Outline each Trypanosoma brucei.
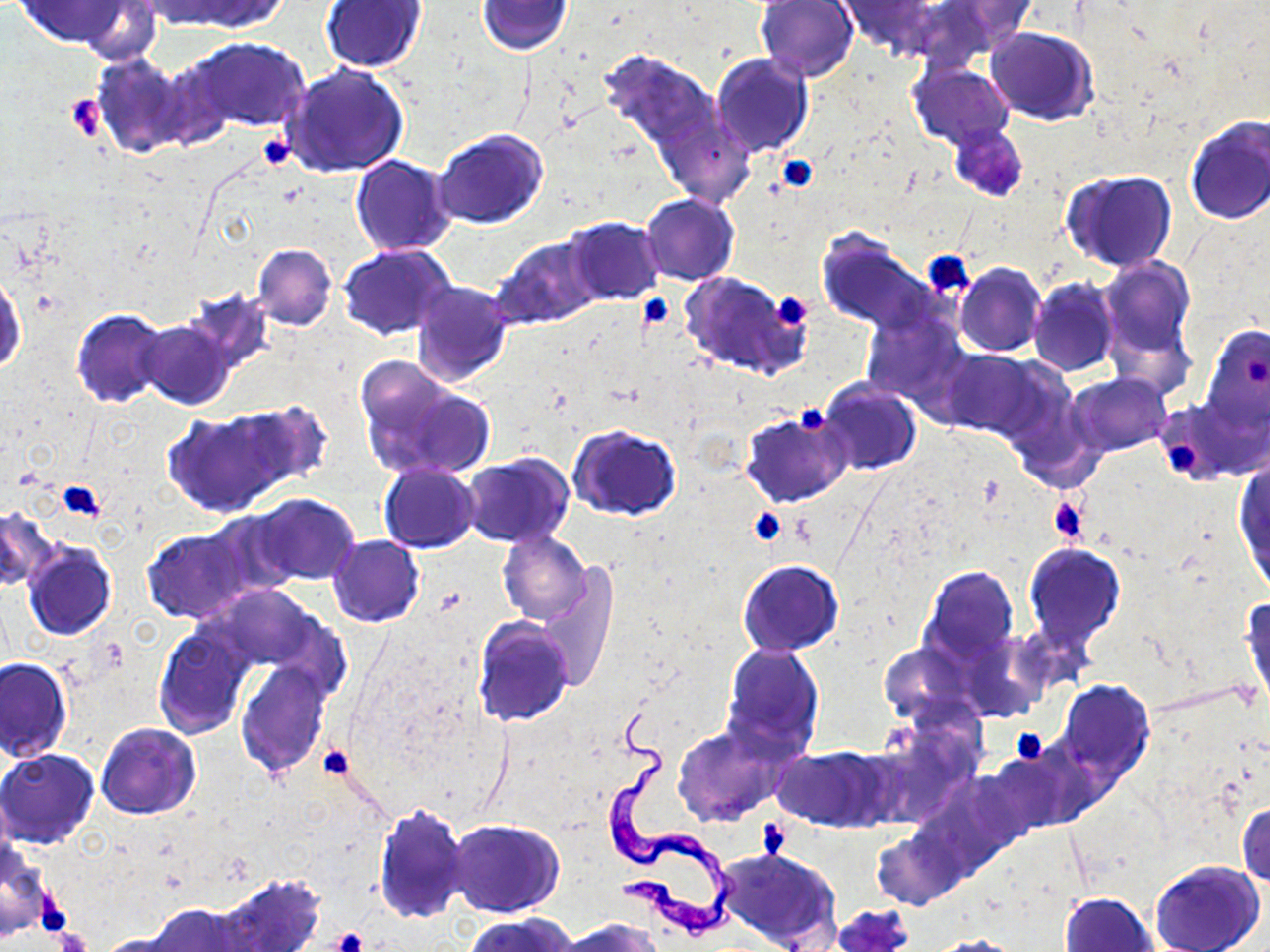

Approximate bounding boxes as (x1, y1, x2, y2) in pixels.
Trypanosoma brucei: (598, 703, 735, 935).

Summary:
  - Uninfected red blood cell locations: (14, 0, 135, 48), (137, 0, 252, 28), (173, 0, 292, 33), (478, 0, 575, 55), (755, 0, 859, 82), (944, 0, 1037, 48), (318, 1, 428, 73), (836, 1, 938, 55), (900, 1, 1021, 62), (74, 2, 163, 66), (985, 26, 1098, 124), (182, 36, 309, 132), (597, 49, 724, 155), (710, 52, 813, 159), (90, 53, 193, 157), (281, 63, 409, 178), (908, 63, 1014, 152), (655, 103, 754, 211), (1184, 115, 1270, 226), (950, 124, 1028, 202), (433, 131, 547, 230), (350, 154, 457, 256), (1062, 169, 1178, 271), (641, 193, 739, 286), (564, 216, 663, 304), (817, 230, 939, 336), (493, 235, 603, 327), (252, 244, 337, 330), (339, 244, 456, 339), (1099, 256, 1196, 369), (955, 263, 1046, 357), (0, 272, 26, 374), (679, 272, 808, 378), (1028, 277, 1119, 377), (410, 280, 514, 387), (181, 289, 276, 380), (72, 307, 171, 409), (861, 308, 970, 406), (138, 321, 234, 409), (1199, 324, 1270, 438), (939, 349, 1042, 439), (354, 363, 493, 482), (1065, 373, 1173, 457), (815, 378, 921, 477), (164, 407, 299, 517), (741, 409, 850, 508), (568, 424, 681, 520), (1234, 450, 1270, 594), (461, 454, 574, 547), (378, 462, 480, 553), (249, 494, 360, 585), (0, 505, 57, 593), (205, 508, 308, 598), (143, 528, 252, 623), (498, 530, 591, 624), (328, 535, 424, 627), (22, 540, 116, 640), (1023, 544, 1126, 651), (737, 559, 843, 656), (536, 564, 618, 692), (919, 564, 1021, 666), (205, 583, 330, 674), (1241, 593, 1269, 712), (472, 616, 575, 725), (153, 623, 255, 740), (879, 640, 977, 726), (721, 644, 824, 757), (0, 658, 73, 762), (234, 661, 331, 778), (1055, 678, 1154, 782), (96, 722, 201, 819), (672, 723, 789, 827), (776, 746, 890, 832), (0, 749, 102, 849), (988, 754, 1084, 836), (1236, 797, 1270, 887), (372, 803, 472, 925), (448, 819, 564, 918), (869, 825, 965, 911), (0, 845, 49, 941), (716, 847, 840, 952), (1149, 859, 1266, 952), (213, 873, 325, 952), (1060, 890, 1161, 951), (143, 901, 255, 952), (465, 913, 577, 952), (560, 917, 660, 952), (93, 930, 196, 952), (925, 935, 1028, 952)
  - Platelet locations: (65, 94, 103, 140), (256, 134, 297, 172), (775, 154, 818, 193), (922, 250, 974, 296), (771, 292, 812, 328), (638, 295, 675, 330), (1244, 353, 1267, 385), (797, 405, 832, 435), (1170, 442, 1197, 479), (56, 482, 106, 521), (1046, 498, 1089, 544), (748, 509, 786, 546), (1008, 727, 1048, 765), (318, 744, 355, 781), (40, 895, 72, 930), (54, 927, 92, 952), (333, 927, 369, 952)
  - Slide-level diagnosis: Trypanosoma brucei
  - Modality: optical microscopy
  - Stain: May-Grünwald-Giemsa
  - Magnification: 1000x
  - Preparation: thin blood smear
  - Image size: 1270×952 pixels
  - Field of view: single